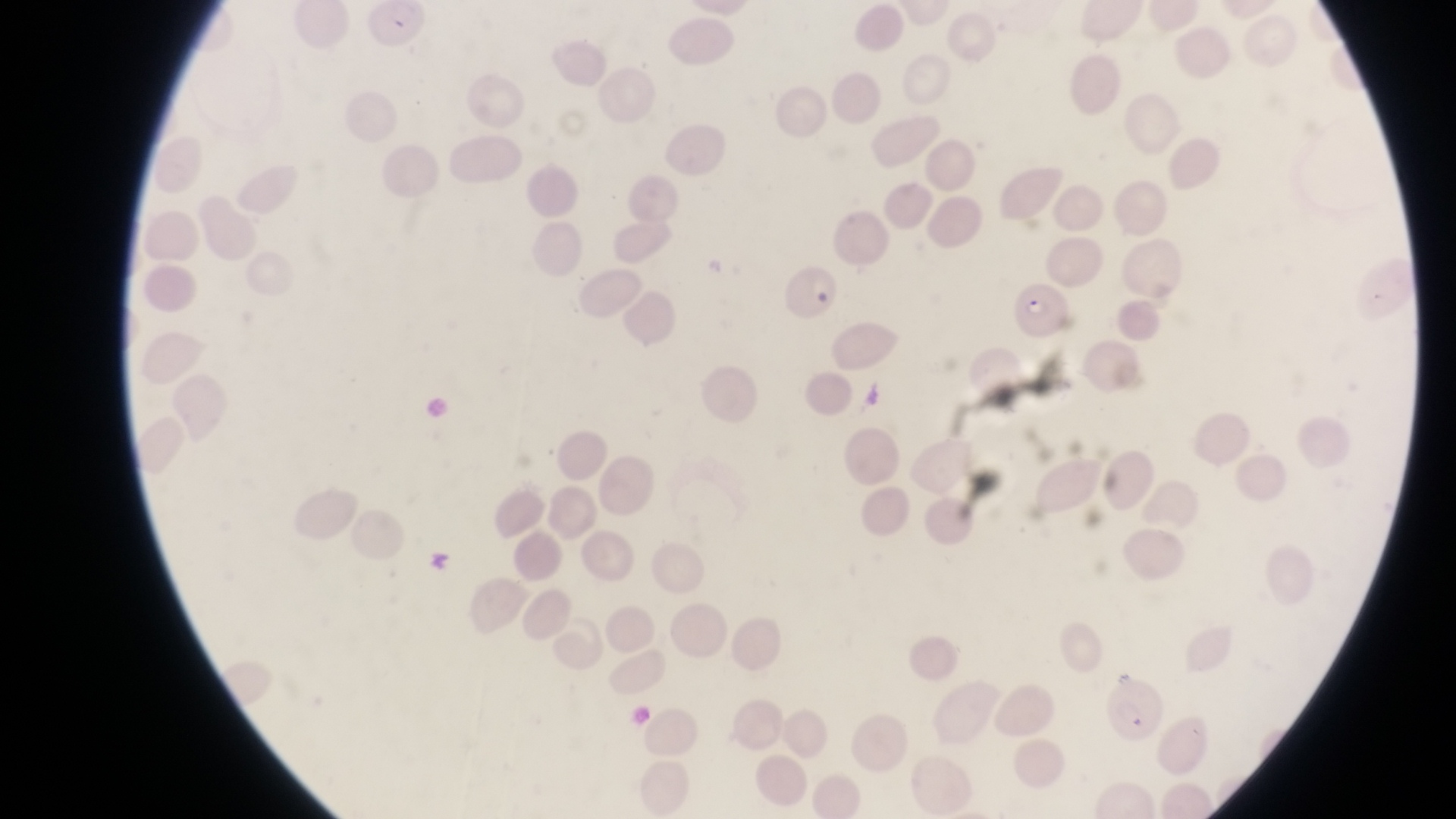

Approximate bounding boxes as (left, top, right, bottom) in pixels.
Summary:
  - Parasitised red blood cell locations: (777, 270, 841, 325), (1010, 280, 1077, 339), (1102, 676, 1166, 743)
  - Image size: 1456×819 pixels
  - Field of view: single
  - Magnification: 1000x
  - Preparation: thin blood film
  - Country: Uganda
  - Capture: smartphone photograph through the eyepiece of an Olympus CX-23 microscope